Describe the morphology of the erythrocytes.
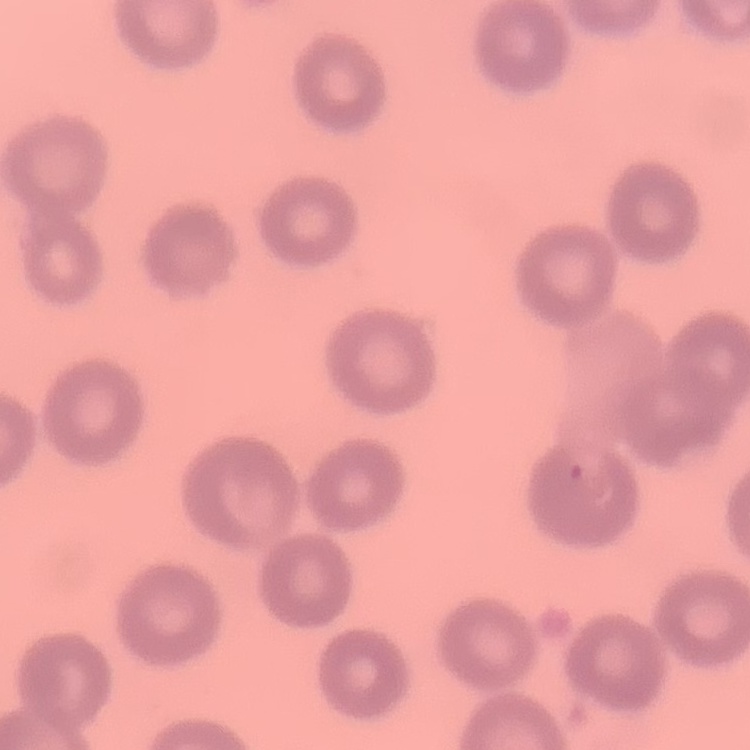

No rouleaux formation.

{
  "image_type": "square crop of a larger photomicrograph",
  "stain": "Field's or Giemsa",
  "preparation": "thin peripheral smear"
}